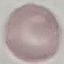
Malaria status: uninfected. Photographed with a smartphone camera at the microscope eyepiece. Giemsa-stained preparation. Thin smear of blood. Cell patch, automatically extracted from a larger field of view and resized to 64 × 64 pixels.